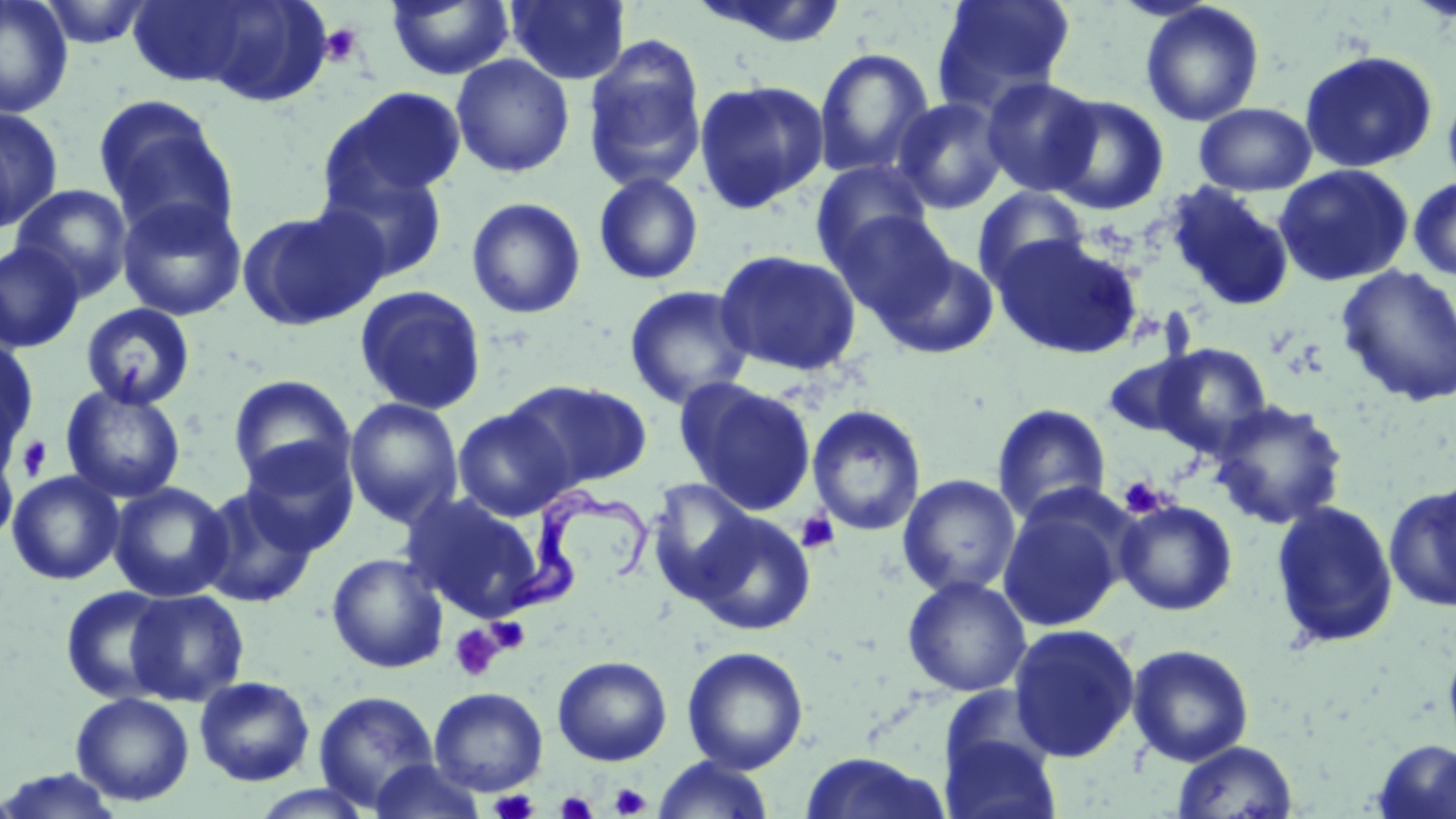
Summary:
  - Coordinate format: approximate bounding boxes as [x1, y1, x2, y2] in pixels
  - Platelet locations: [320, 24, 364, 66], [15, 435, 53, 481], [1118, 476, 1166, 518], [796, 511, 841, 553], [487, 616, 531, 654], [449, 624, 504, 682], [609, 783, 651, 818], [489, 788, 539, 819], [555, 790, 598, 818]
  - Uninfected red blood cell locations: [0, 0, 74, 118], [37, 0, 157, 49], [385, 0, 515, 81], [505, 0, 631, 85], [688, 0, 851, 50], [931, 0, 1077, 113], [1139, 2, 1265, 127], [126, 3, 273, 87], [582, 36, 707, 194], [813, 47, 935, 179], [1299, 49, 1438, 173], [451, 54, 575, 178], [980, 76, 1103, 197], [693, 78, 830, 213], [1442, 84, 1456, 197], [321, 87, 467, 208], [1043, 94, 1169, 215], [93, 96, 236, 237], [892, 97, 1009, 214], [1194, 102, 1317, 196], [0, 107, 63, 233], [810, 160, 932, 270], [1273, 164, 1414, 287], [322, 167, 449, 283], [593, 172, 704, 286], [1408, 176, 1456, 281], [1164, 182, 1296, 313], [11, 184, 134, 300], [971, 186, 1091, 292], [116, 195, 248, 322], [465, 196, 586, 319], [238, 206, 388, 332], [829, 209, 959, 324], [993, 234, 1142, 360], [0, 241, 84, 353], [876, 247, 999, 359], [714, 249, 862, 377], [1335, 265, 1456, 407], [354, 285, 487, 415], [624, 285, 754, 409], [80, 303, 196, 411], [0, 335, 38, 462], [1150, 343, 1274, 456], [1102, 350, 1210, 440], [228, 374, 355, 489], [677, 378, 817, 515], [508, 379, 652, 490], [60, 383, 186, 503], [343, 397, 464, 527], [1210, 400, 1348, 530], [991, 403, 1112, 525], [806, 404, 927, 536], [452, 406, 575, 521], [1, 439, 19, 550], [239, 439, 359, 555], [7, 470, 124, 585], [897, 474, 1021, 598], [646, 479, 757, 599], [108, 481, 233, 602], [1384, 482, 1456, 615], [195, 485, 319, 608], [401, 493, 544, 620], [997, 495, 1129, 633], [1115, 499, 1238, 616], [1269, 499, 1399, 650], [692, 511, 816, 635], [327, 553, 448, 673], [902, 575, 1032, 698], [60, 585, 177, 704], [126, 588, 249, 706], [1007, 622, 1141, 763], [1442, 631, 1456, 757], [1126, 643, 1255, 766], [682, 645, 809, 774], [552, 655, 672, 765], [194, 675, 315, 786], [429, 687, 548, 796], [313, 690, 439, 811], [71, 692, 194, 806], [940, 728, 1062, 819], [1371, 738, 1456, 818], [1171, 741, 1299, 818], [797, 751, 951, 819], [651, 756, 776, 819], [367, 758, 488, 819], [0, 769, 124, 818], [249, 785, 377, 819]
  - Trypanosoma brucei locations: [504, 484, 654, 618]
  - Slide-level diagnosis: Trypanosoma brucei
  - Stain: May-Grünwald-Giemsa
  - Preparation: thin blood smear
  - Modality: optical microscopy
  - Field of view: single
  - Image size: 1456×819 pixels
  - Magnification: 1000x